Describe the morphology of the erythrocytes.
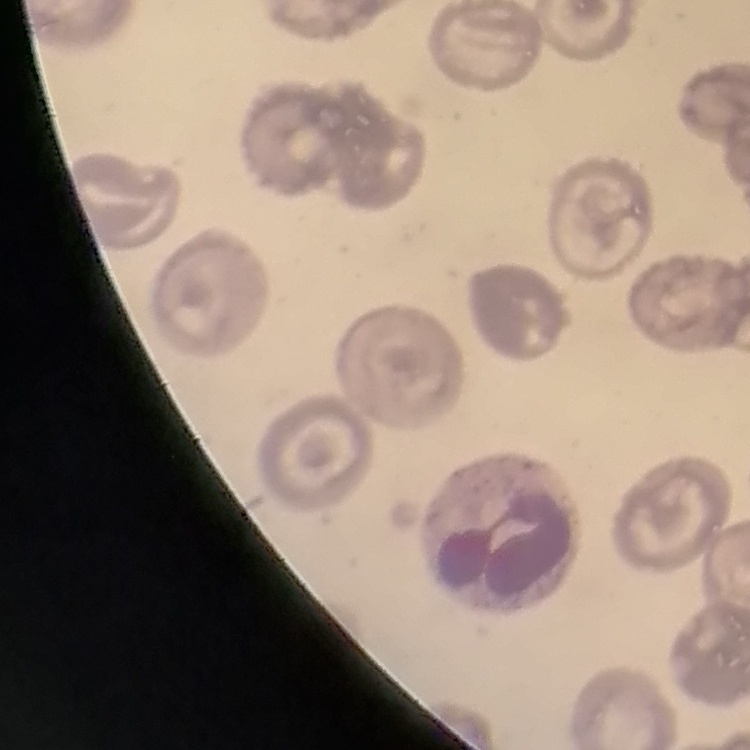

They show no rouleaux formation.

Stained with either Field's or Giemsa. One tile cut from a larger photomicrograph. Thin blood smear.